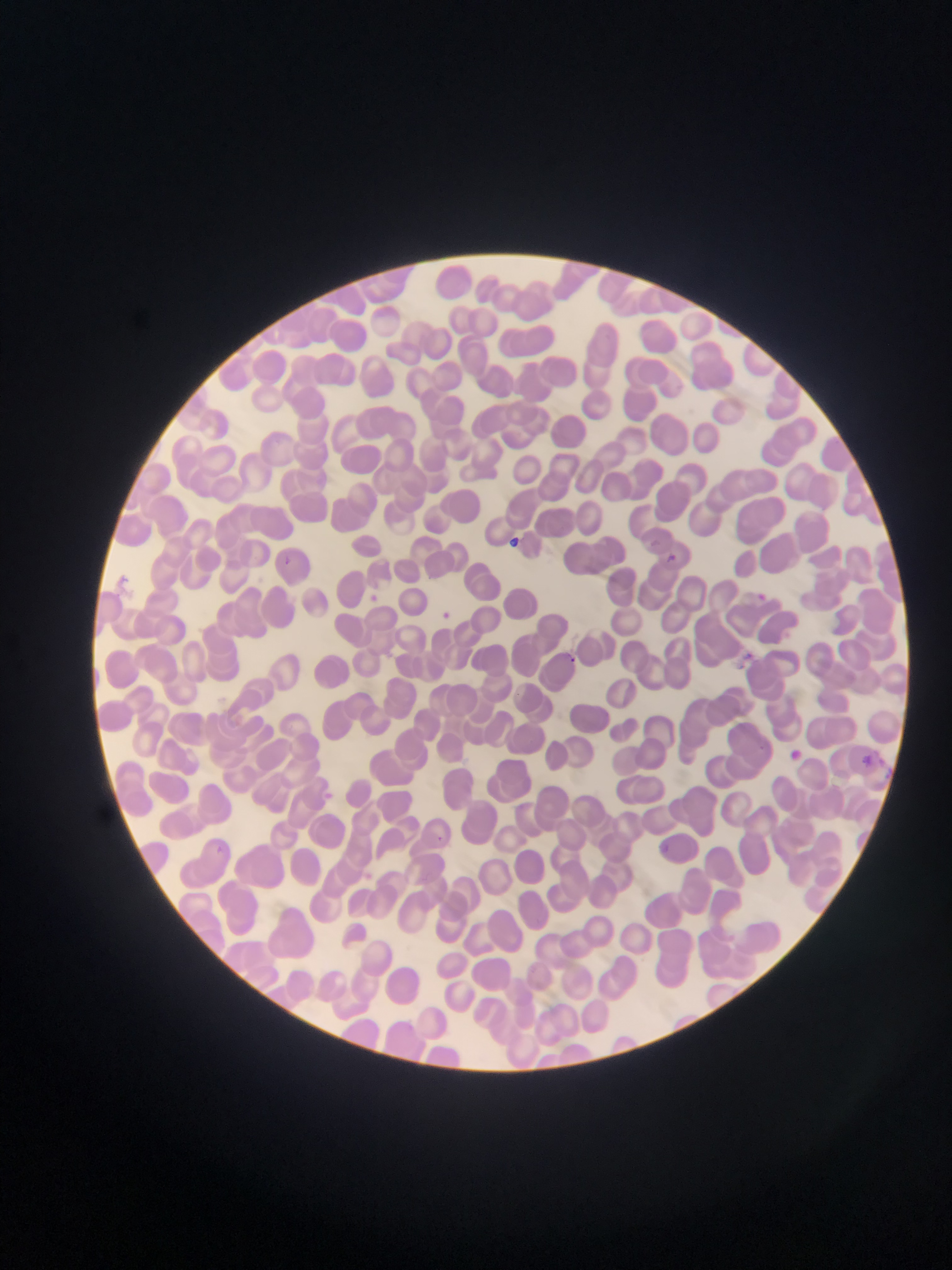
Plasmodium parasite locations = approximate bounding boxes as [left, top, right, bottom] in pixels: [652, 537, 661, 546], [658, 554, 681, 566], [284, 555, 298, 566], [754, 586, 776, 607], [442, 609, 452, 620], [743, 644, 756, 657], [570, 653, 580, 665], [789, 749, 811, 766], [864, 749, 881, 761], [432, 832, 456, 854], [212, 845, 227, 857]
preparation = thin blood film
field of view = single
country = Ghana
image size = 952×1270 pixels
capture = mobile-phone photograph through a microscope